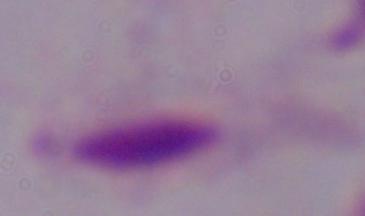

magnification = 1000x
modality = photomicrograph
identification = trichomonad